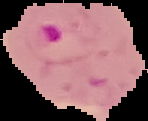 Image is 148×121 pixels. Result: malaria parasites detected. From a thin blood smear. Segmented cell region on a black background.